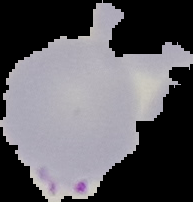

{
  "image_size": "193×202 pixels",
  "preparation": "thin blood smear",
  "malaria_status": "parasitized",
  "image_type": "segmented cell region on a black background"
}